Outline platelets.
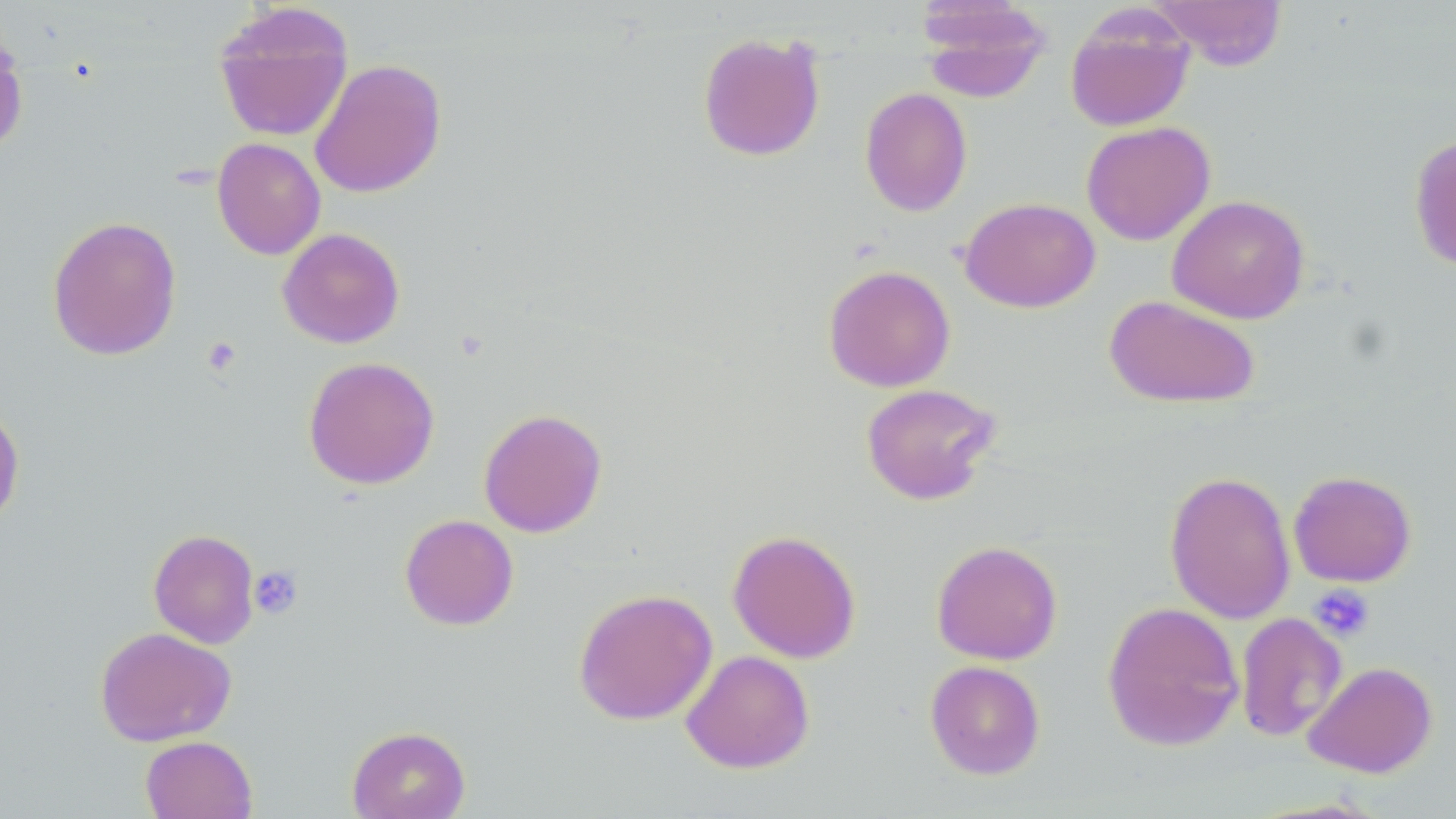
Approximate bounding boxes as named x1/y1/x2/y2 corners in pixels.
Platelets: (x1=201, y1=336, x2=242, y2=377), (x1=248, y1=565, x2=303, y2=619), (x1=1309, y1=584, x2=1375, y2=642).

Uninfected red blood cell locations: (x1=1148, y1=0, x2=1289, y2=71), (x1=918, y1=1, x2=1053, y2=100), (x1=213, y1=3, x2=354, y2=142), (x1=1065, y1=6, x2=1196, y2=133), (x1=697, y1=31, x2=826, y2=162), (x1=0, y1=32, x2=29, y2=155), (x1=309, y1=58, x2=447, y2=199), (x1=859, y1=87, x2=973, y2=216), (x1=1081, y1=121, x2=1216, y2=245), (x1=1408, y1=134, x2=1456, y2=273), (x1=212, y1=137, x2=326, y2=260), (x1=1167, y1=194, x2=1310, y2=324), (x1=959, y1=196, x2=1100, y2=313), (x1=47, y1=215, x2=182, y2=361), (x1=277, y1=228, x2=405, y2=349), (x1=823, y1=264, x2=956, y2=392), (x1=1104, y1=294, x2=1260, y2=408), (x1=302, y1=356, x2=440, y2=490), (x1=860, y1=383, x2=1003, y2=505), (x1=0, y1=400, x2=25, y2=531), (x1=478, y1=408, x2=607, y2=537), (x1=1164, y1=470, x2=1296, y2=624), (x1=1288, y1=470, x2=1417, y2=587), (x1=399, y1=514, x2=519, y2=631), (x1=148, y1=528, x2=259, y2=648), (x1=727, y1=529, x2=862, y2=663), (x1=931, y1=540, x2=1063, y2=665), (x1=573, y1=587, x2=718, y2=726), (x1=1101, y1=600, x2=1244, y2=751), (x1=1234, y1=612, x2=1347, y2=742), (x1=94, y1=626, x2=236, y2=747), (x1=680, y1=650, x2=815, y2=774), (x1=924, y1=659, x2=1046, y2=780), (x1=1303, y1=660, x2=1438, y2=778), (x1=346, y1=725, x2=470, y2=819), (x1=140, y1=735, x2=257, y2=818). Slide-level diagnosis: negative for blood parasites. Thin blood smear. Image is 1456×819 pixels. Captured at 1000x magnification. May-Grünwald-Giemsa-stained preparation. Optical microscopy. Single field of view.